Identify the parasite.
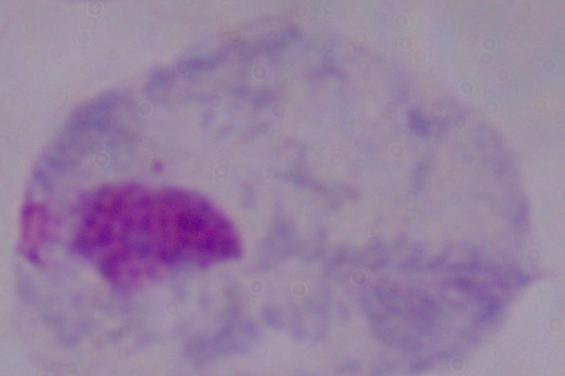

This is a trichomonad.

Captured at 1000x magnification. Photomicrograph.